Assess this cell for malaria.
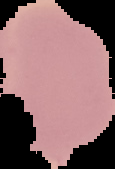

Uninfected.

Segmented cell region on a black background. From a thin blood smear. Image is 115×169 pixels.